Report the malaria status of this cell.
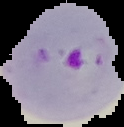
It is parasitized.

Summary:
  - Image type: segmented cell region on a black background
  - Preparation: thin blood film
  - Image size: 124×127 pixels